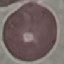
Summary:
  - Result: negative for malaria parasites
  - Image type: automatically extracted cell patch, resized to 64 × 64 pixels
  - Stain: Giemsa
  - Capture: smartphone through the microscope eyepiece
  - Preparation: thin smear